Report the malaria status of this cell.
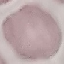
It is uninfected.

Summary:
  - Stain: Giemsa
  - Capture: smartphone camera at the microscope eyepiece
  - Image type: automatically extracted cell patch, resized to 64 × 64 pixels
  - Preparation: thin smear